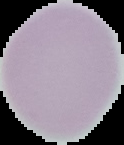
From a thin blood smear. Cell region segmented out of the field of view; the surrounding area is masked to black. Image is 124×145 pixels. Result: no malaria parasites detected.